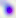
modality = micrograph
identification = Toxoplasma gondii
magnification = 400x